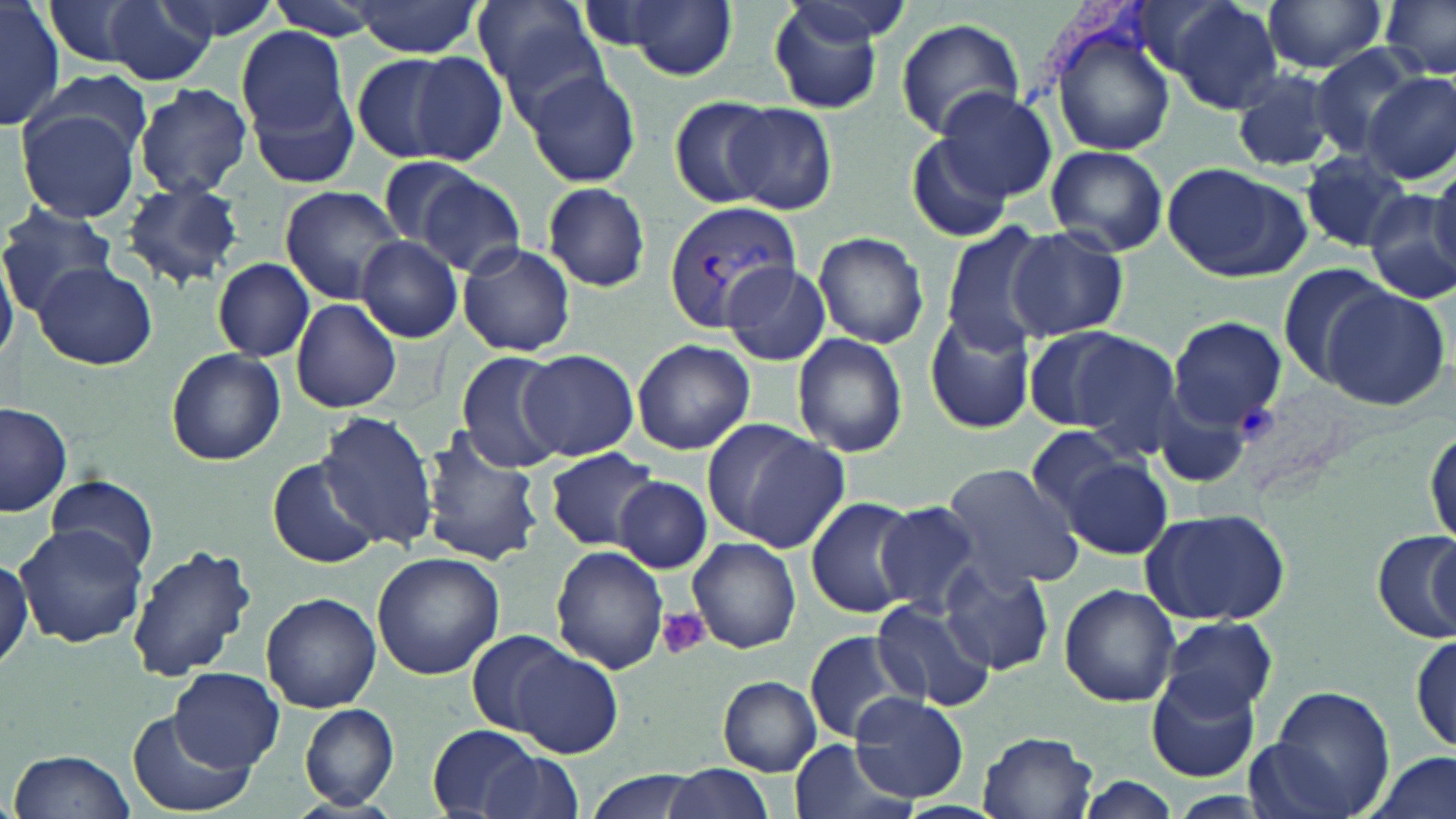 Approximate bounding boxes as [x1, y1, x2, y2] in pixels. Uninfected red blood cell locations: [1, 0, 62, 131], [43, 0, 152, 67], [103, 0, 216, 86], [153, 0, 281, 40], [261, 0, 383, 42], [471, 0, 605, 110], [598, 0, 740, 81], [765, 0, 885, 114], [1154, 0, 1289, 108], [1261, 0, 1390, 74], [1381, 0, 1456, 79], [348, 2, 485, 57], [895, 18, 1026, 139], [1048, 23, 1178, 156], [231, 27, 351, 147], [1308, 44, 1426, 158], [348, 50, 471, 164], [400, 50, 510, 167], [240, 65, 364, 195], [24, 69, 154, 162], [1230, 69, 1340, 172], [523, 70, 642, 186], [1366, 72, 1455, 184], [133, 84, 253, 199], [930, 87, 1058, 204], [666, 97, 777, 208], [725, 103, 837, 216], [19, 107, 143, 223], [904, 133, 1015, 242], [1045, 144, 1169, 256], [1297, 151, 1414, 254], [373, 153, 490, 255], [1159, 161, 1308, 281], [1428, 164, 1456, 278], [411, 171, 525, 277], [118, 178, 246, 289], [540, 181, 652, 292], [278, 186, 406, 304], [1361, 187, 1456, 305], [1, 202, 117, 312], [937, 222, 1055, 356], [1007, 227, 1129, 342], [813, 231, 929, 349], [359, 237, 462, 346], [456, 243, 576, 356], [210, 259, 315, 362], [32, 260, 157, 371], [721, 260, 831, 367], [1276, 262, 1393, 387], [1322, 286, 1450, 409], [291, 299, 402, 413], [923, 309, 1034, 433], [1169, 316, 1287, 433], [1037, 327, 1180, 449], [792, 333, 909, 460], [632, 339, 755, 455], [164, 349, 286, 466], [456, 350, 568, 473], [519, 350, 639, 460], [1, 400, 74, 519], [315, 408, 438, 554], [703, 419, 850, 551], [1426, 424, 1456, 551], [1024, 426, 1130, 521], [414, 428, 545, 568], [544, 447, 660, 550], [1063, 458, 1171, 558], [268, 459, 381, 568], [939, 464, 1086, 590], [46, 474, 160, 578], [613, 477, 713, 574], [804, 496, 922, 618], [873, 502, 984, 613], [1141, 507, 1291, 627], [15, 526, 150, 649], [1414, 528, 1452, 640], [1371, 532, 1455, 646], [688, 538, 801, 653], [125, 544, 258, 684], [552, 545, 669, 674], [0, 551, 33, 673], [373, 553, 505, 681], [939, 560, 1054, 674], [1059, 583, 1180, 706], [261, 592, 380, 712], [871, 600, 994, 708], [1160, 617, 1278, 719], [467, 627, 571, 736], [803, 631, 919, 745], [1411, 631, 1454, 755], [510, 646, 623, 759], [170, 668, 284, 773], [1144, 670, 1260, 782], [718, 676, 822, 776], [1258, 688, 1393, 817], [849, 691, 970, 803], [299, 704, 399, 810], [125, 711, 254, 818], [426, 725, 551, 817], [977, 731, 1099, 818], [788, 737, 912, 819], [7, 749, 138, 819], [475, 752, 583, 819], [1362, 752, 1456, 819], [660, 762, 771, 819], [584, 767, 700, 819], [1070, 776, 1183, 819]. Plasmodium vivax-infected red blood cell locations: [664, 199, 799, 332]. Platelet locations: [658, 609, 710, 661]. Slide-level diagnosis: Plasmodium vivax. One field of a larger specimen. Thin blood smear. May-Grünwald-Giemsa stain. Captured at 1000x magnification. Light microscopy. Image is 1456×819 pixels.